Locate every leukocyte (white blood cell).
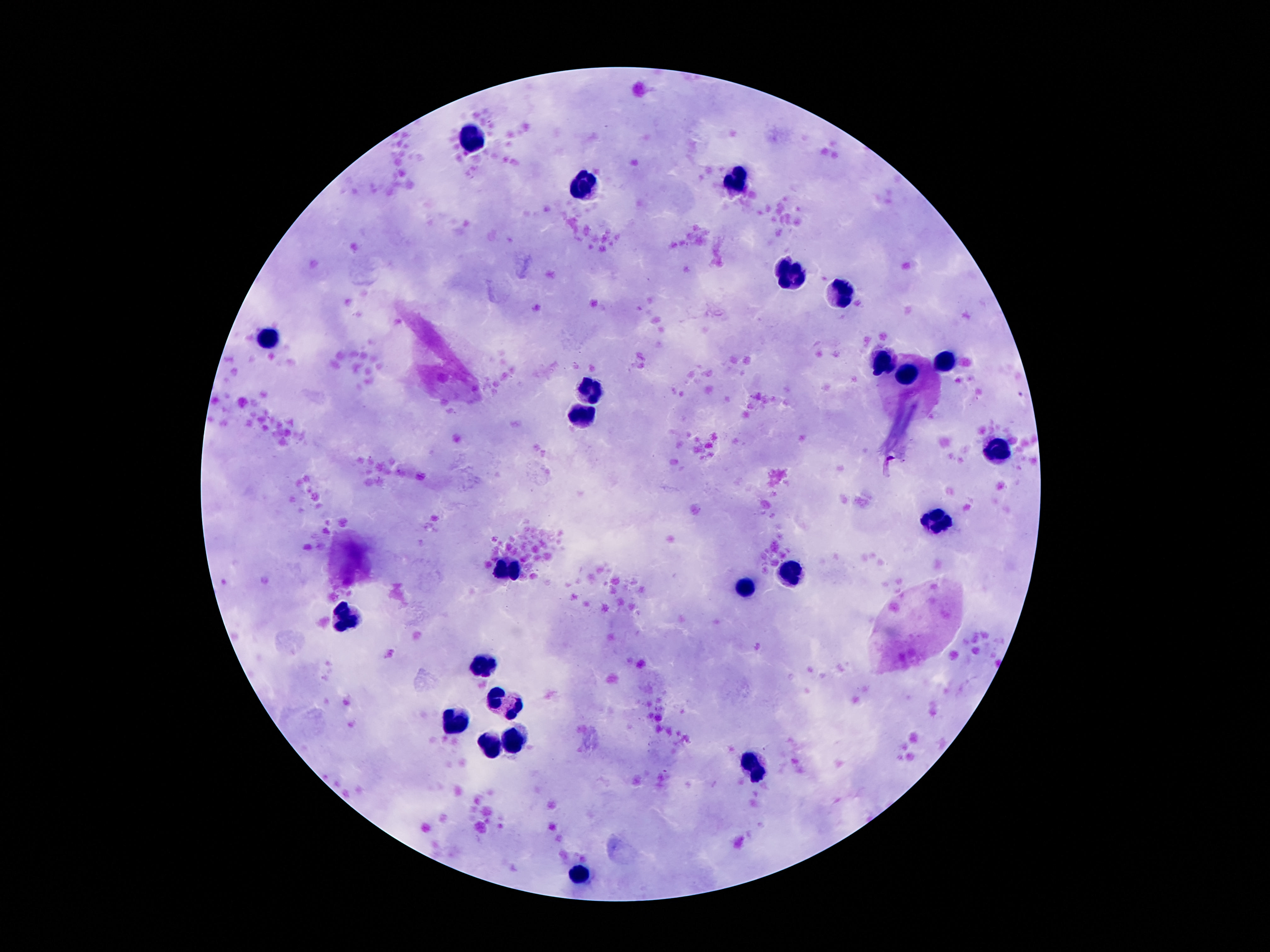

Approximate centers as (x, y) in pixels.
Leukocytes: (477, 137), (734, 184), (585, 188), (790, 274), (843, 294), (269, 337), (947, 361), (884, 363), (908, 374), (591, 386), (583, 414), (998, 447), (936, 522), (509, 570), (790, 574), (746, 588), (346, 615), (482, 663), (493, 696), (516, 709), (456, 719), (518, 742), (490, 745), (753, 768), (579, 874).

Patient malaria status: not infected. Smartphone photograph taken through the microscope eyepiece. Single field of view. Giemsa stain. 100x magnification. Image is 1270×952 pixels. Thick peripheral-blood smear.